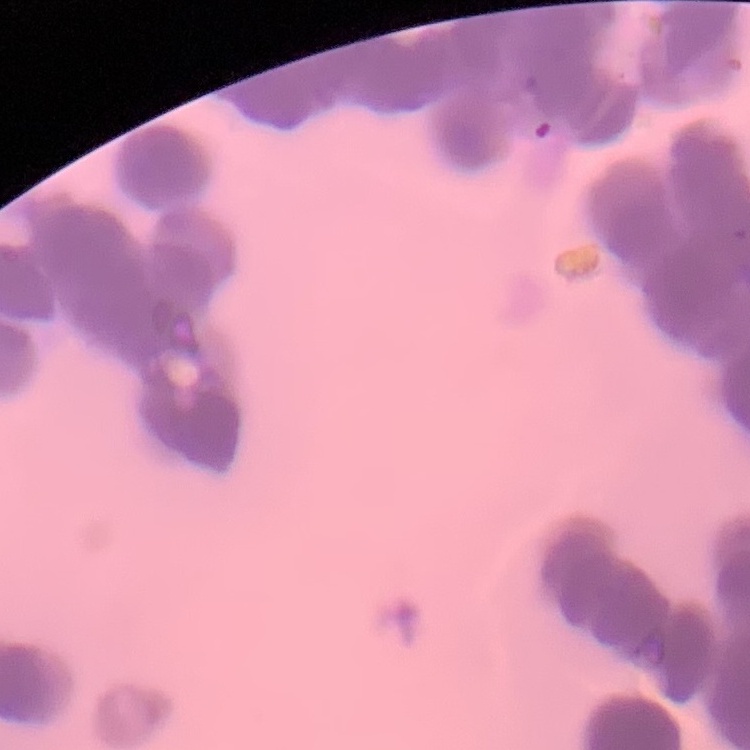
Summary:
  - Erythrocyte morphology: rouleaux formation
  - Preparation: thin blood film
  - Image type: one tile cut from a larger photomicrograph
  - Stain: Field's or Giemsa